Describe the morphology of the red blood cells.
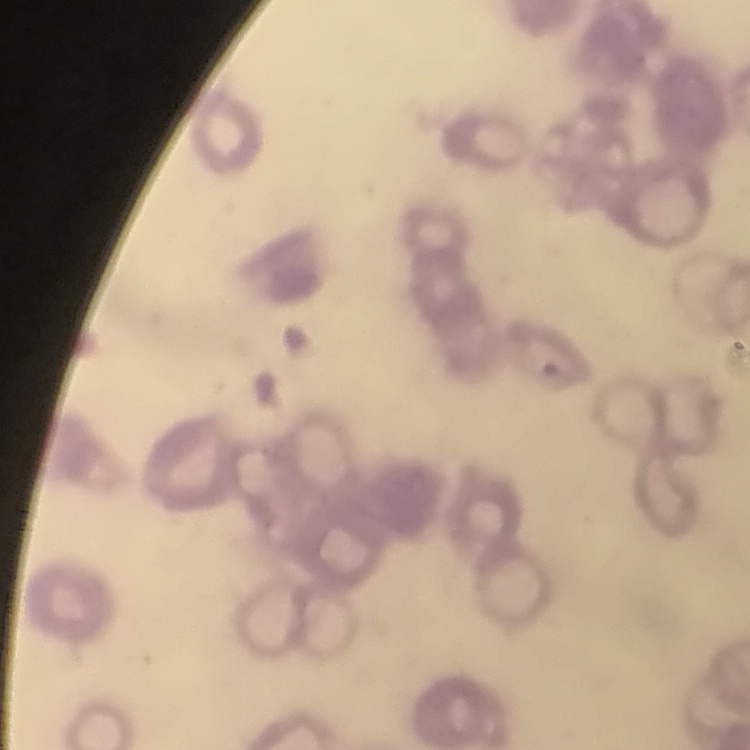

They show rouleaux formation.

stain = Field's or Giemsa
image type = one tile cut from a larger photomicrograph
preparation = thin peripheral smear